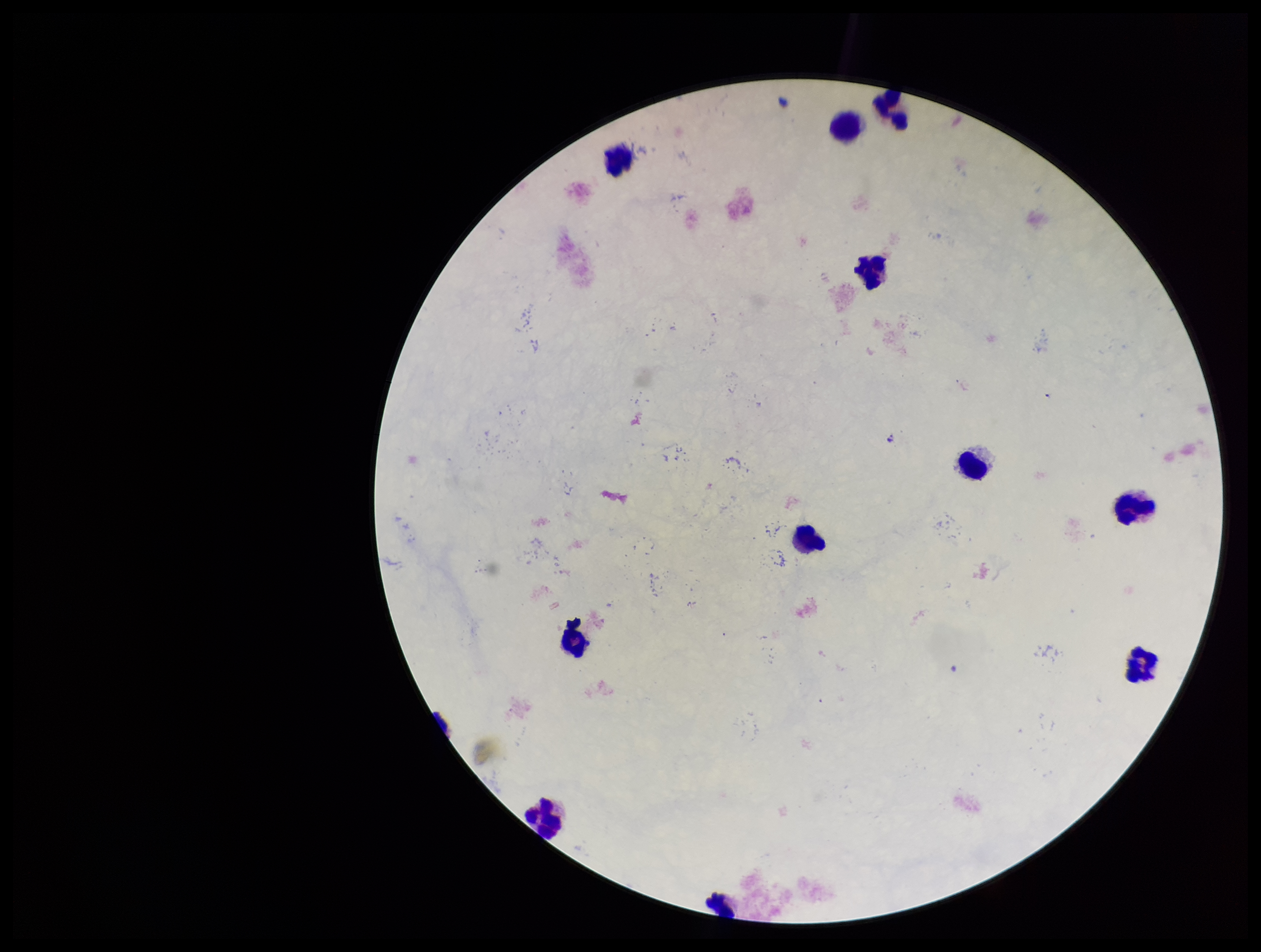
Photographed through the microscope eyepiece with a smartphone camera. Giemsa stain. Parasite count: 0. Leukocyte count: 11. Single field of view. Patient malaria status: negative. Image is 1261×952 pixels. Plasmodium parasites: none detected. Preparation: thick smear.